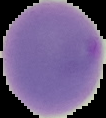

malaria status = parasitized
preparation = thin blood smear
image type = segmented cell region on a black background
image size = 106×118 pixels